Report the malaria status of this cell.
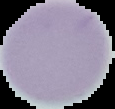

Uninfected.

Summary:
  - Image size: 115×109 pixels
  - Image type: segmented cell region with the area outside set to black
  - Preparation: thin blood smear